Locate every Plasmodium parasite.
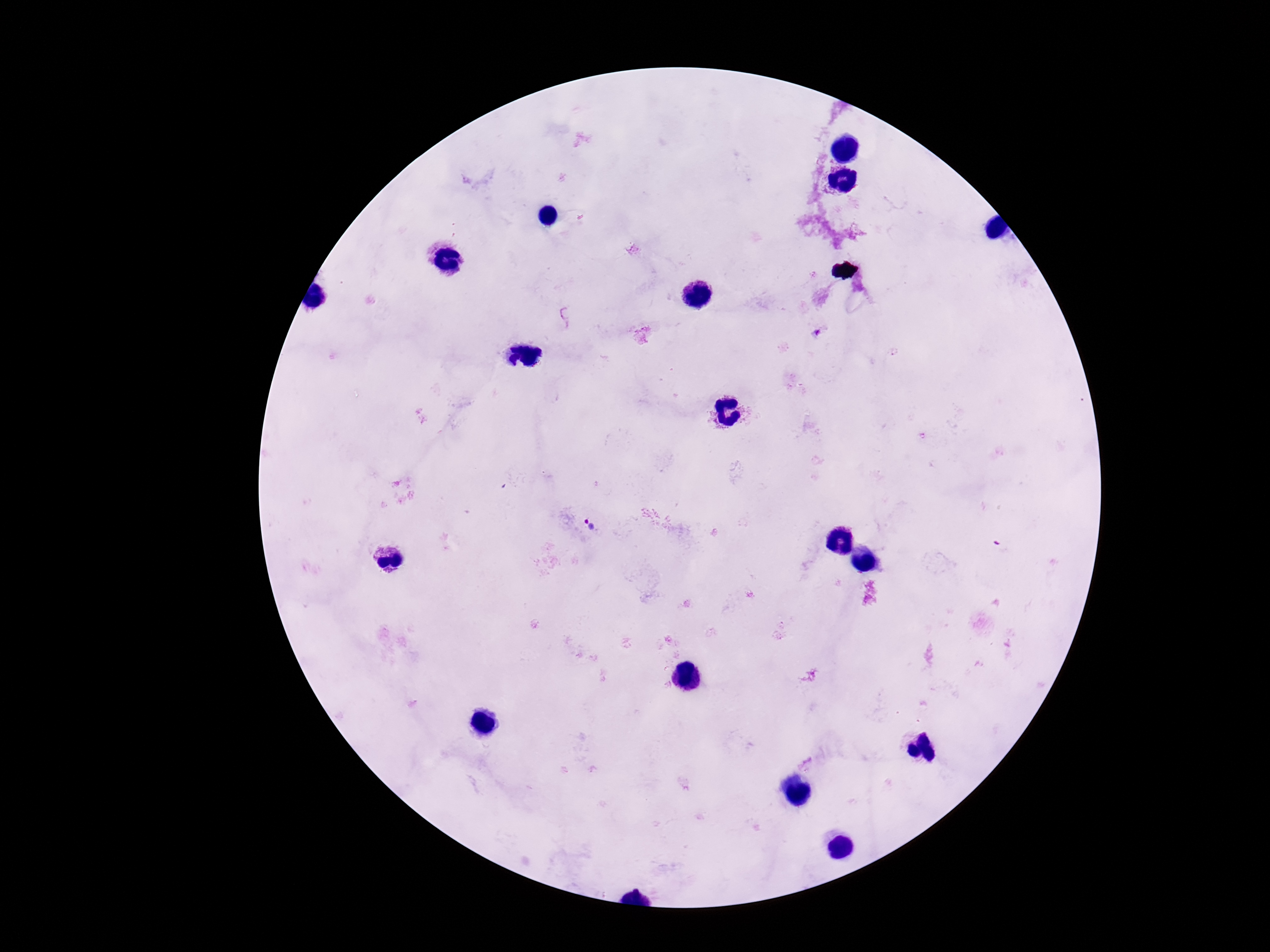

Approximate object centers, in pixels from the top-left corner.
Plasmodium parasites: (x=567, y=316), (x=818, y=335), (x=589, y=525).

Photographed through the microscope eyepiece with a smartphone camera. Patient malaria status: positive. Thick blood film. Image is 1270×952 pixels. Giemsa stain. 100x magnification. One field from this slide.